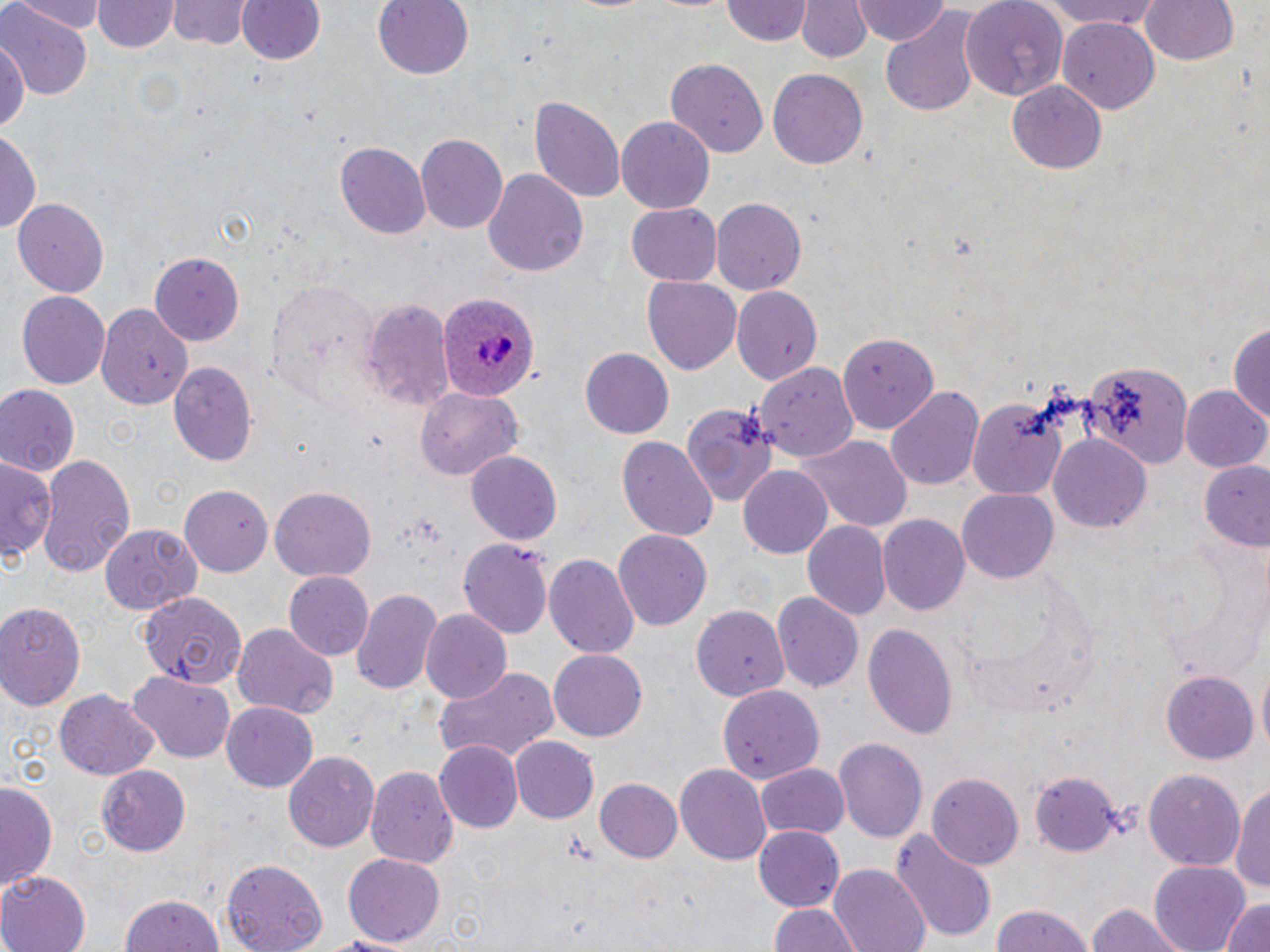

Approximate bounding boxes as [x1, y1, x2, y2] in pixels. Plasmodium ovale-infected red blood cell locations: [435, 293, 537, 401]. Uninfected red blood cell locations: [7, 0, 107, 30], [170, 0, 248, 50], [236, 0, 323, 67], [373, 0, 472, 80], [960, 0, 1069, 102], [1045, 0, 1163, 32], [1140, 0, 1239, 67], [95, 1, 177, 54], [722, 1, 812, 46], [795, 1, 872, 63], [852, 1, 949, 46], [2, 4, 89, 102], [879, 9, 982, 118], [1057, 16, 1160, 109], [0, 36, 29, 142], [664, 56, 767, 156], [768, 68, 868, 168], [1008, 81, 1106, 174], [530, 95, 625, 206], [617, 115, 717, 212], [0, 130, 40, 235], [417, 133, 508, 234], [337, 141, 430, 239], [484, 167, 588, 279], [12, 196, 108, 297], [710, 197, 806, 295], [627, 204, 722, 285], [150, 253, 243, 343], [643, 277, 741, 376], [266, 280, 377, 406], [731, 288, 822, 384], [16, 289, 113, 389], [362, 299, 457, 411], [98, 300, 193, 406], [1231, 321, 1270, 435], [837, 331, 940, 434], [579, 348, 674, 440], [1084, 359, 1194, 471], [167, 362, 258, 467], [757, 362, 857, 463], [0, 384, 80, 478], [886, 385, 985, 492], [1181, 387, 1270, 474], [415, 390, 521, 480], [969, 396, 1069, 498], [680, 401, 779, 504], [1050, 434, 1151, 531], [617, 435, 719, 543], [797, 435, 911, 532], [465, 449, 563, 545], [36, 452, 135, 578], [1, 455, 57, 560], [1200, 462, 1270, 549], [739, 467, 831, 557], [179, 485, 271, 576], [270, 487, 375, 582], [959, 488, 1058, 583], [879, 514, 969, 616], [804, 520, 891, 621], [100, 522, 202, 612], [613, 530, 712, 631], [456, 537, 554, 640], [544, 553, 638, 660], [282, 571, 372, 660], [352, 588, 442, 697], [138, 590, 248, 691], [772, 593, 864, 696], [1, 601, 85, 710], [690, 605, 787, 701], [420, 611, 512, 705], [862, 620, 959, 738], [231, 622, 340, 719], [548, 647, 646, 739], [433, 664, 560, 767], [1257, 664, 1270, 757], [1161, 669, 1257, 763], [127, 674, 237, 762], [716, 683, 826, 803], [56, 687, 160, 780], [221, 703, 317, 791], [510, 737, 598, 823], [835, 738, 927, 844], [436, 740, 524, 832], [284, 749, 380, 852], [675, 763, 771, 865], [366, 764, 460, 868], [755, 764, 849, 840], [97, 767, 190, 855], [1030, 769, 1122, 856], [1144, 770, 1245, 872], [928, 774, 1023, 868], [1, 777, 60, 898], [594, 778, 682, 863], [1232, 778, 1270, 897], [753, 826, 844, 911], [892, 829, 997, 946], [343, 853, 442, 948], [222, 859, 328, 952], [1150, 860, 1251, 951], [832, 864, 930, 952], [0, 870, 91, 952], [118, 892, 224, 952], [1219, 897, 1270, 952], [1086, 903, 1189, 952], [768, 904, 860, 952], [987, 905, 1096, 952], [305, 932, 421, 950]. Slide-level diagnosis: Plasmodium ovale. One field of a larger specimen. Light microscopy. 1000x magnification. Image is 1270×952 pixels. May-Grünwald-Giemsa stain. Thin blood film.